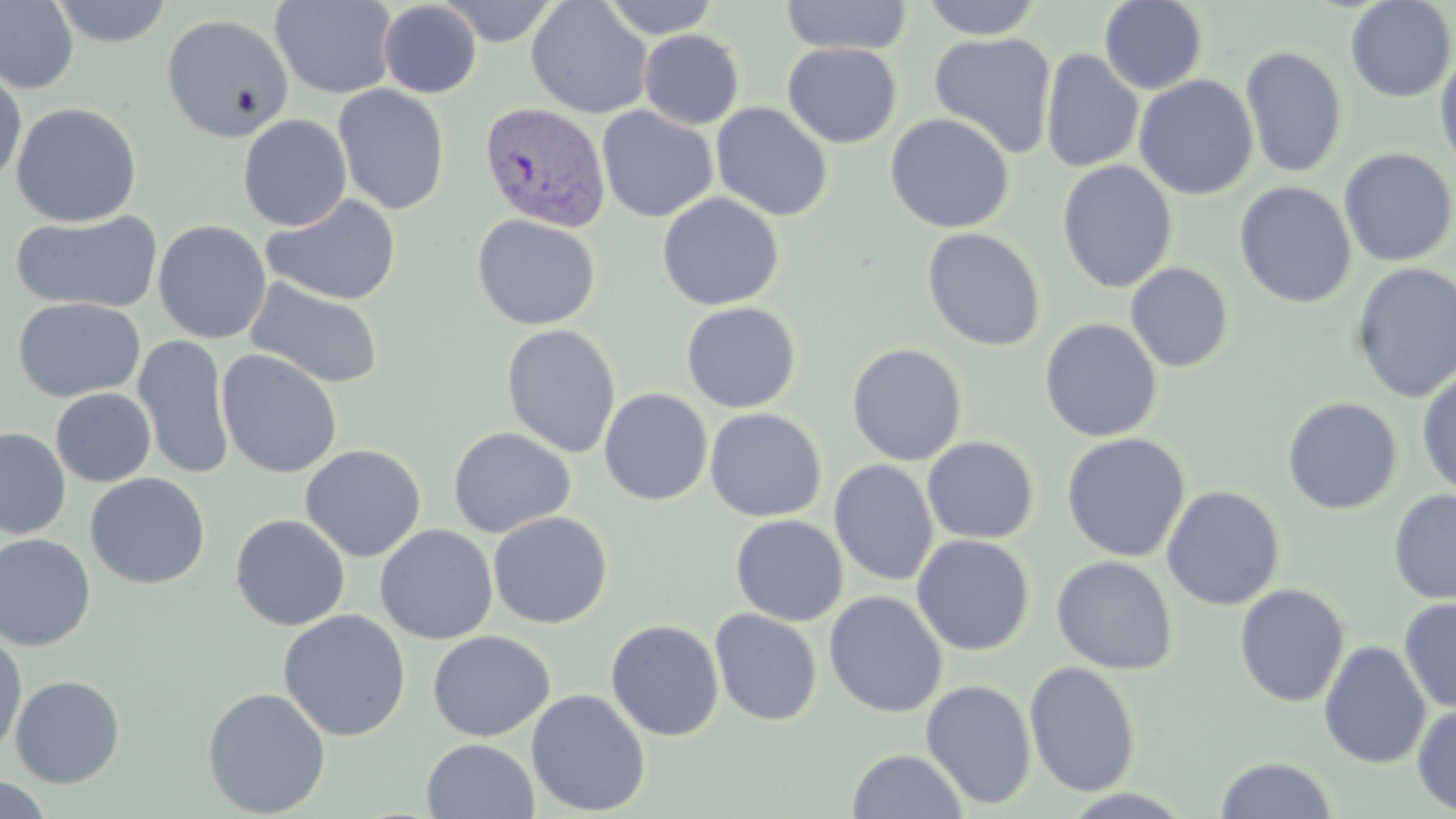

Summary:
  - Coordinate format: approximate bounding boxes as (x1, y1, x2, y2) in pixels
  - Uninfected red blood cell locations: (0, 0, 79, 95), (48, 0, 174, 47), (270, 0, 398, 99), (436, 0, 562, 46), (600, 0, 722, 39), (780, 0, 913, 57), (921, 0, 1043, 40), (1098, 0, 1209, 94), (1345, 0, 1455, 103), (526, 1, 653, 119), (377, 2, 482, 98), (161, 13, 294, 143), (639, 29, 744, 129), (929, 32, 1058, 159), (782, 42, 902, 149), (1240, 46, 1347, 179), (1041, 48, 1144, 173), (1434, 50, 1456, 175), (0, 62, 27, 187), (1133, 75, 1259, 200), (333, 84, 450, 215), (10, 102, 142, 228), (711, 102, 833, 222), (596, 105, 718, 223), (885, 113, 1014, 234), (237, 114, 352, 231), (1338, 147, 1455, 268), (1057, 160, 1178, 294), (1234, 181, 1356, 309), (657, 192, 784, 311), (261, 193, 401, 305), (10, 209, 164, 314), (472, 213, 601, 331), (153, 220, 271, 344), (922, 227, 1045, 352), (1125, 261, 1234, 373), (1352, 263, 1456, 403), (246, 277, 385, 390), (12, 297, 146, 403), (680, 302, 801, 413), (1039, 318, 1163, 443), (501, 323, 621, 458), (132, 335, 235, 480), (847, 342, 968, 466), (216, 349, 343, 479), (1417, 367, 1456, 498), (50, 388, 156, 487), (598, 388, 712, 505), (1282, 397, 1402, 515), (705, 407, 826, 522), (448, 426, 576, 538), (0, 427, 71, 539), (1060, 433, 1190, 563), (922, 436, 1039, 544), (301, 444, 426, 561), (829, 459, 939, 586), (85, 473, 210, 589), (1161, 485, 1285, 611), (1389, 489, 1456, 606), (488, 511, 612, 629), (230, 513, 350, 631), (730, 514, 848, 626), (374, 524, 498, 645), (0, 534, 95, 650), (911, 534, 1035, 656), (1051, 556, 1178, 675), (1234, 584, 1350, 708), (824, 591, 947, 718), (1398, 596, 1456, 714), (709, 607, 823, 726), (278, 609, 411, 741), (605, 619, 724, 740), (428, 630, 554, 741), (0, 631, 27, 762), (1319, 640, 1431, 769), (1024, 661, 1141, 797), (10, 675, 125, 788), (920, 679, 1037, 810), (202, 686, 331, 818), (526, 689, 650, 816), (1412, 704, 1456, 816), (421, 738, 539, 819), (846, 748, 968, 819), (1214, 756, 1339, 818), (0, 775, 57, 819)
  - Plasmodium vivax-infected red blood cell locations: (478, 102, 612, 232)
  - Slide-level diagnosis: Plasmodium vivax
  - Modality: optical microscopy
  - Stain: May-Grünwald-Giemsa
  - Field of view: single
  - Image size: 1456×819 pixels
  - Preparation: thin blood smear
  - Magnification: 1000x